Classify this cell by malaria status.
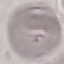

It is uninfected.

{
  "image_type": "cell patch, automatically extracted from a larger field of view and resized to 64 × 64 pixels",
  "capture": "smartphone through the microscope eyepiece",
  "preparation": "thin blood smear",
  "stain": "Giemsa"
}